State which cell type is depicted.
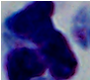
This is a leukocyte.

Photomicrograph. 1000x magnification.